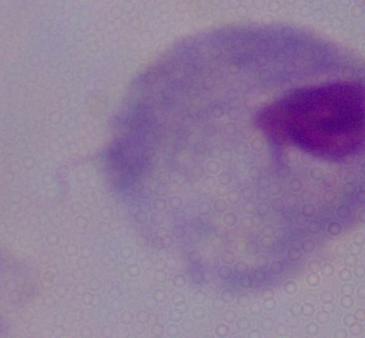

magnification = 1000x
modality = photomicrograph
identification = trichomonad